Evaluate for Plasmodium parasites.
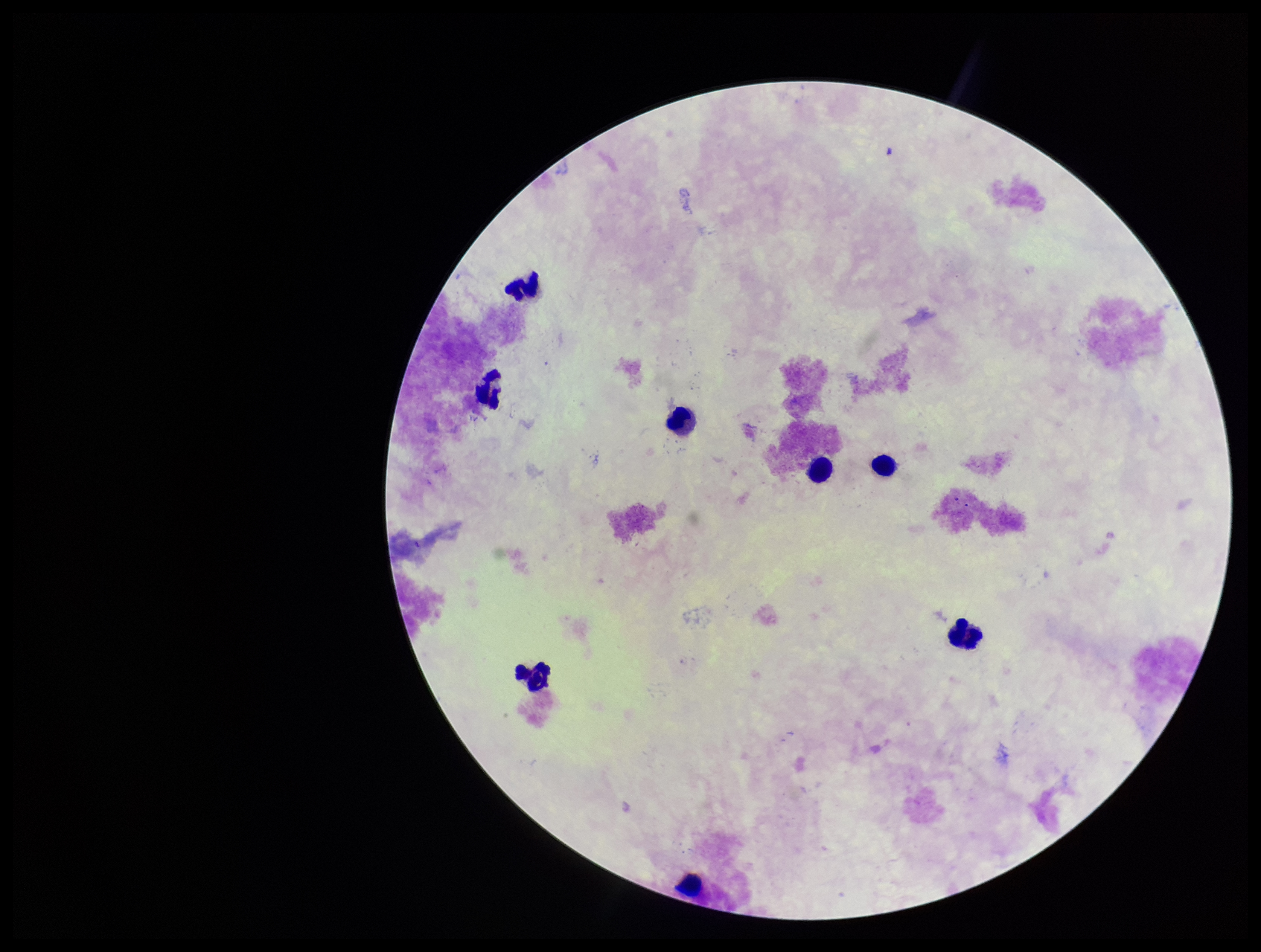
None detected.

Summary:
  - Field of view: single
  - Preparation: thick
  - Parasite count: 0
  - Image size: 1261×952 pixels
  - Patient malaria status: negative
  - Capture: smartphone photograph through the microscope eyepiece
  - Stain: Giemsa
  - Leukocyte count: 8